Assess this cell for malaria.
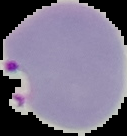

Parasitized.

Summary:
  - Preparation: thin blood film
  - Image type: cell region segmented out of the field of view; surrounding area masked to black
  - Image size: 127×136 pixels